Locate every leukocyte (white blood cell).
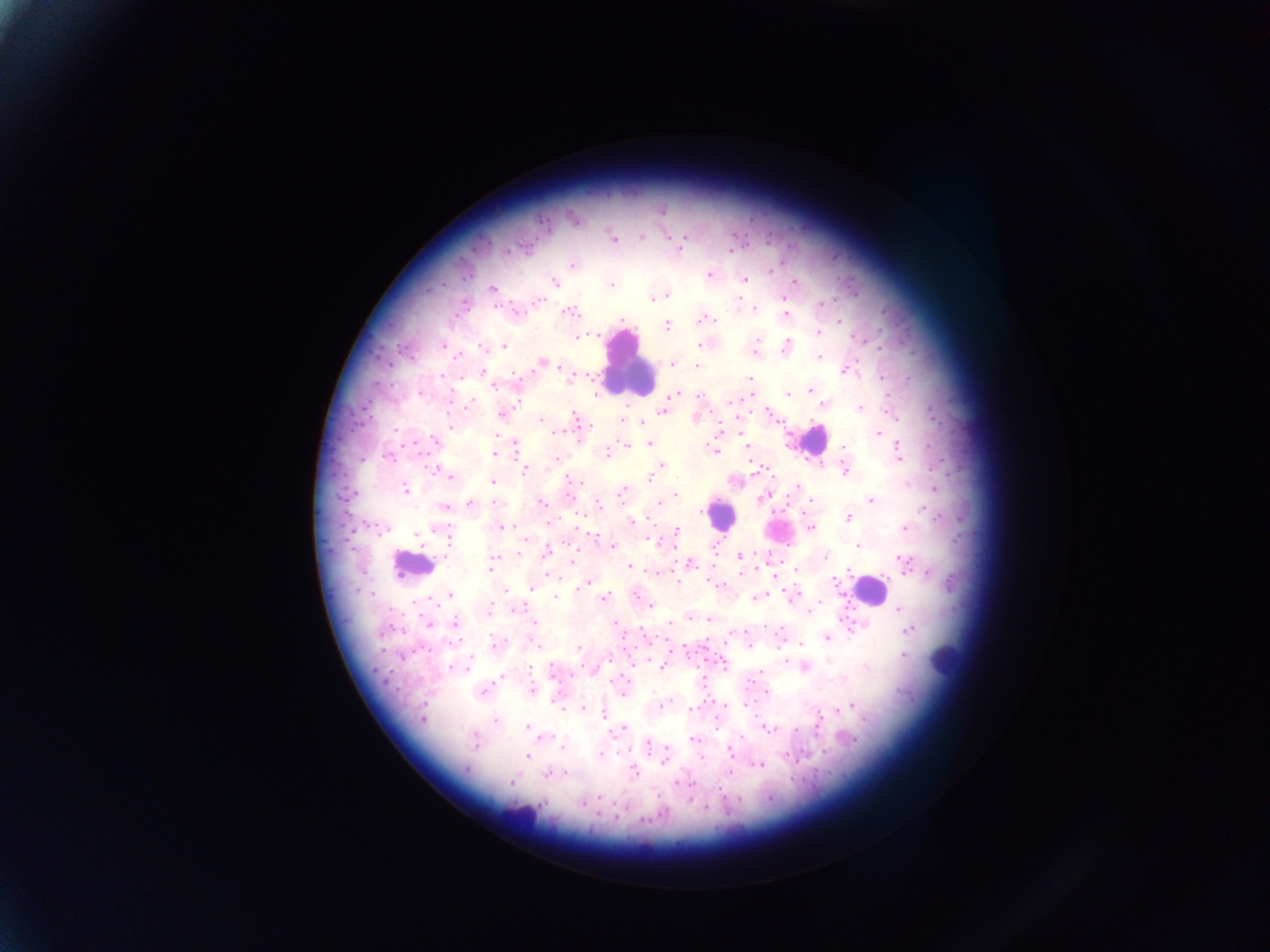

Approximate centers as (x, y) in pixels.
Leukocytes: (629, 365), (812, 440), (724, 513), (411, 565), (869, 591), (943, 660), (517, 817).

Summary:
  - Plasmodium parasite locations: (662, 209), (641, 237), (685, 237), (613, 239), (506, 251), (730, 252), (572, 265), (771, 270), (709, 275), (745, 279), (554, 282), (795, 282), (611, 285), (492, 288), (667, 295), (785, 298), (652, 299), (537, 301), (822, 304), (754, 309), (515, 312), (570, 312), (785, 315), (705, 319), (623, 320), (714, 320), (839, 322), (667, 326), (818, 332), (578, 336), (595, 336), (757, 339), (442, 345), (699, 345), (504, 347), (483, 348), (786, 348), (755, 353), (457, 357), (818, 357), (543, 361), (672, 364), (696, 366), (559, 367), (483, 368), (845, 370), (483, 372), (514, 373), (441, 376), (572, 378), (750, 378), (882, 378), (494, 386), (809, 390), (788, 393), (420, 394), (596, 395), (676, 395), (450, 397), (470, 401), (730, 402), (824, 404), (859, 407), (662, 412), (623, 413), (768, 413), (501, 414), (575, 419), (541, 420), (622, 420), (641, 422), (451, 427), (719, 429), (556, 433), (878, 434), (496, 435), (435, 440), (515, 444), (649, 444), (625, 445), (748, 447), (843, 447), (898, 447), (611, 449), (713, 450), (606, 453), (494, 454), (388, 457), (898, 458), (557, 459), (662, 465), (844, 470), (525, 471), (449, 477), (649, 478), (492, 481), (573, 481), (908, 484), (798, 486), (935, 488), (405, 490), (622, 493), (352, 494), (676, 495), (762, 498), (811, 500), (871, 500), (494, 502), (659, 502), (541, 503), (598, 504), (469, 505), (444, 507), (925, 511), (702, 512), (937, 516), (848, 517), (632, 520), (437, 526), (502, 527), (382, 529), (810, 529), (904, 529), (676, 530), (416, 535), (447, 537), (654, 541), (612, 546), (858, 546), (546, 552), (520, 554), (738, 556), (825, 556), (495, 557), (572, 560), (904, 562), (690, 563), (712, 564), (630, 566), (489, 567), (797, 570), (848, 571), (904, 571), (654, 572), (741, 573), (927, 573), (552, 575), (834, 581), (677, 582), (585, 583), (532, 588), (578, 588), (504, 590), (794, 592), (635, 594), (450, 595), (556, 596), (761, 596), (604, 598), (756, 599), (820, 602), (651, 605), (899, 608), (489, 609), (517, 609), (808, 611), (690, 617), (710, 619), (670, 622), (455, 623), (535, 623), (616, 624), (428, 625), (909, 629), (744, 632), (827, 638), (493, 641), (532, 642), (800, 644), (578, 648), (903, 655), (470, 659), (609, 659), (786, 662), (724, 664), (451, 666), (465, 666), (661, 666), (805, 667), (530, 668), (552, 670), (760, 671), (502, 678), (532, 689), (483, 692), (766, 692), (623, 694), (744, 703), (662, 705), (852, 706), (561, 709), (583, 709), (690, 709), (838, 710), (604, 715), (422, 718), (864, 720), (495, 721), (716, 723), (818, 724), (526, 726), (765, 726), (624, 727), (769, 729), (545, 736), (742, 736), (693, 739), (853, 740), (475, 742), (648, 745), (561, 746), (617, 751), (666, 751), (730, 751), (824, 752), (600, 754), (526, 756), (701, 758), (663, 761), (759, 764), (466, 770), (633, 771), (730, 772), (566, 773), (546, 776), (511, 783), (679, 783), (599, 798), (543, 803), (581, 803), (705, 807), (644, 819)
  - Preparation: thick blood film
  - Field of view: single
  - Country: Ghana
  - Capture: mobile-phone photograph through a microscope
  - Image size: 1270×952 pixels